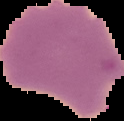
{
  "preparation": "thin blood smear",
  "result": "malaria parasites identified",
  "image_type": "segmented cell region with the area outside set to black",
  "image_size": "124×121 pixels"
}